Outline each uninfected red blood cell.
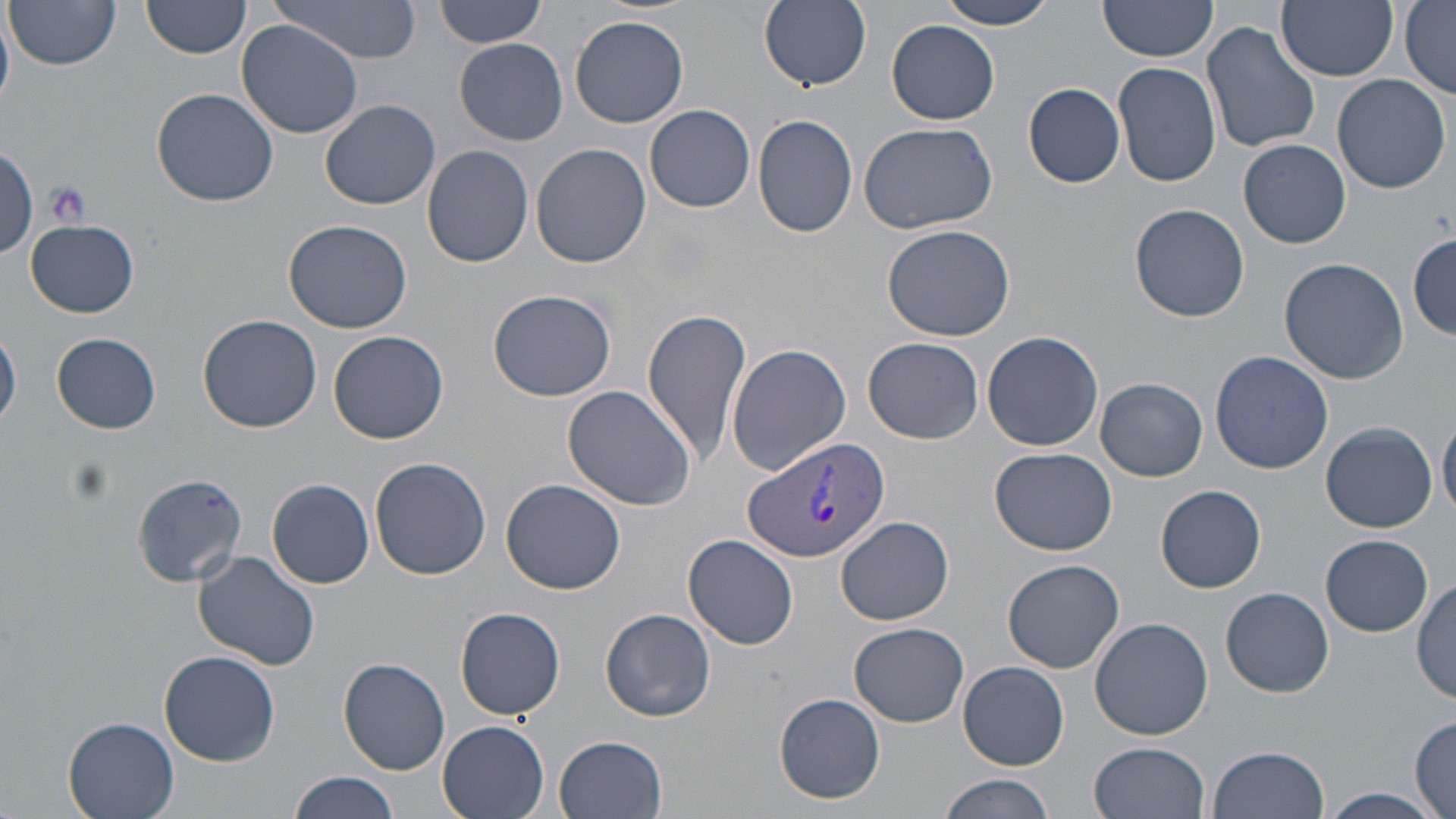
Approximate bounding boxes as [x1, y1, x2, y2] in pixels.
Uninfected red blood cells: [7, 0, 121, 71], [142, 0, 251, 59], [271, 0, 424, 63], [436, 0, 548, 47], [759, 0, 872, 90], [938, 0, 1059, 29], [1277, 0, 1397, 82], [1097, 1, 1220, 66], [1400, 2, 1456, 96], [0, 9, 16, 108], [571, 15, 689, 128], [236, 19, 365, 138], [887, 20, 1000, 124], [1202, 22, 1320, 154], [454, 38, 568, 146], [1113, 61, 1221, 187], [1332, 72, 1452, 193], [1024, 82, 1125, 188], [152, 90, 278, 207], [322, 100, 441, 209], [644, 104, 756, 213], [750, 115, 859, 240], [860, 122, 997, 234], [1240, 139, 1351, 248], [0, 141, 39, 263], [531, 142, 652, 268], [421, 144, 534, 267], [1129, 204, 1250, 322], [284, 218, 413, 333], [25, 219, 139, 317], [882, 224, 1016, 342], [1409, 232, 1454, 338], [1279, 258, 1409, 384], [487, 289, 616, 402], [642, 308, 753, 461], [198, 314, 323, 432], [1, 327, 22, 432], [329, 329, 450, 444], [982, 330, 1104, 452], [53, 332, 162, 433], [863, 337, 983, 443], [727, 343, 852, 475], [1210, 352, 1334, 473], [1096, 377, 1207, 481], [561, 385, 697, 510], [1439, 412, 1456, 521], [1320, 422, 1437, 533], [990, 447, 1118, 556], [370, 457, 490, 580], [130, 472, 248, 585], [268, 478, 374, 588], [502, 479, 624, 595], [1157, 485, 1266, 593], [837, 515, 953, 625], [1321, 534, 1431, 635], [684, 535, 799, 650], [193, 552, 322, 671], [1002, 559, 1124, 673], [1413, 575, 1455, 703], [1223, 586, 1335, 696], [454, 606, 566, 720], [599, 608, 717, 722], [1090, 617, 1213, 740], [848, 623, 970, 727], [159, 649, 281, 767], [339, 657, 450, 774], [959, 661, 1068, 769], [774, 692, 885, 804], [63, 716, 181, 819], [1409, 716, 1456, 817], [437, 720, 552, 819], [555, 734, 669, 819], [1091, 742, 1211, 819], [1209, 744, 1330, 819], [288, 770, 399, 819], [937, 773, 1055, 819], [1317, 786, 1442, 819].

Summary:
  - Plasmodium vivax-infected red blood cell locations: [741, 436, 891, 564]
  - Platelet locations: [44, 180, 91, 228]
  - Slide-level diagnosis: Plasmodium vivax
  - Image size: 1456×819 pixels
  - Preparation: thin blood smear
  - Modality: light microscopy
  - Field of view: one of a larger specimen
  - Magnification: 1000x
  - Stain: May-Grünwald-Giemsa